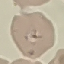
Malaria status: uninfected. Thin smear of blood. Automatically extracted cell patch, resized to 64 × 64 pixels. Acquired by smartphone through the microscope eyepiece. Giemsa-stained preparation.